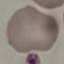

malaria status = uninfected
capture = smartphone through the microscope eyepiece
stain = Giemsa
preparation = thin blood film
image type = automatically extracted cell patch, resized to 64 × 64 pixels